Comment on the morphology of the erythrocytes.
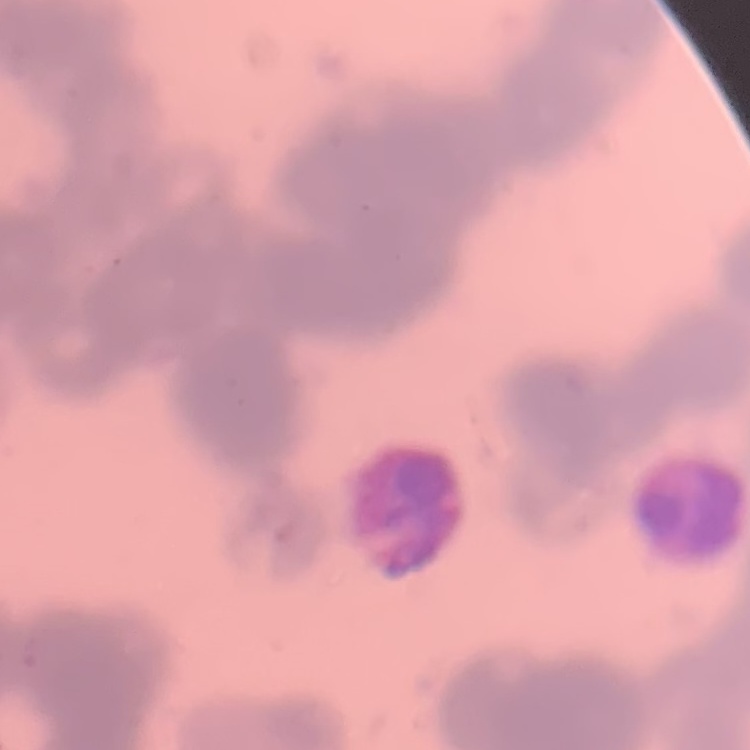

Rouleaux formation.

stain = Field's or Giemsa
image type = square crop of a larger photomicrograph
preparation = thin blood smear